Comment on the morphology of the red blood cells.
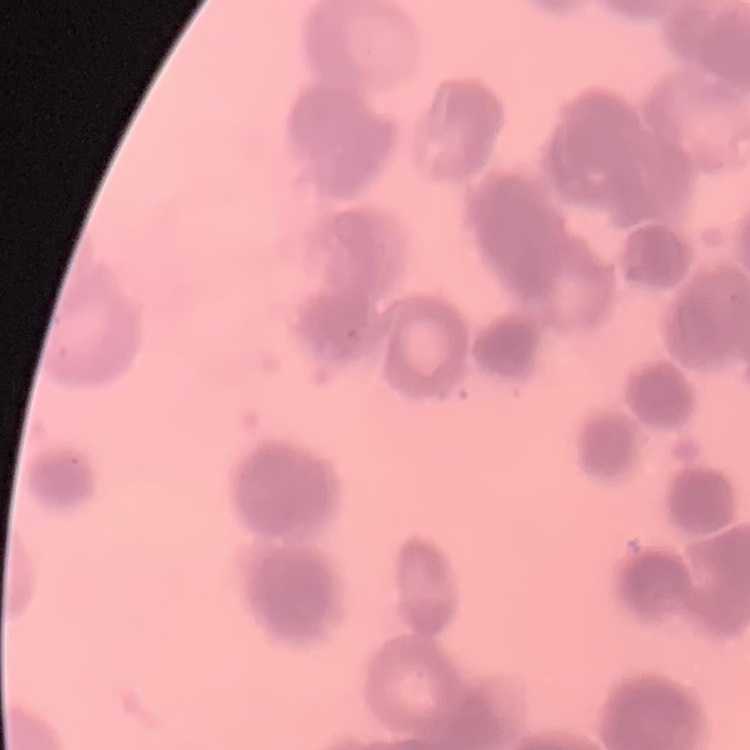
Rouleaux formation.

Summary:
  - Stain: Field's or Giemsa
  - Image type: one tile cut from a larger photomicrograph
  - Preparation: thin blood film